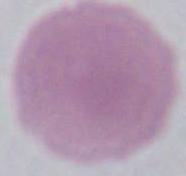

Summary:
  - Magnification: 1000x
  - Modality: micrograph
  - Identification: erythrocyte